Name the cell type shown.
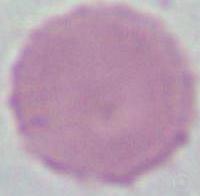

This is an erythrocyte.

Summary:
  - Modality: photomicrograph
  - Magnification: 1000x